Classify this cell by malaria status.
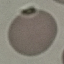
It is uninfected.

Acquired by smartphone through the microscope eyepiece. Automatically extracted cell patch, resized to 64 × 64 pixels. Thin blood film. Giemsa-stained preparation.